Identify the parasite.
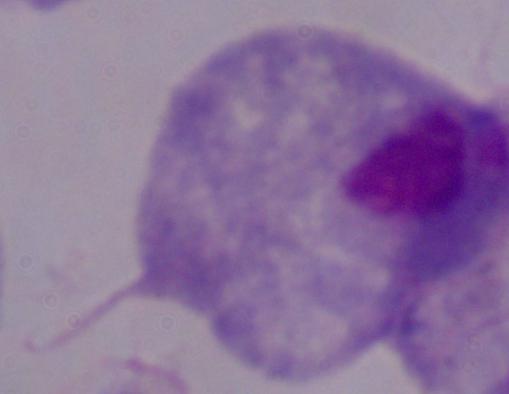

A trichomonad.

Photomicrograph. Captured at 1000x magnification.